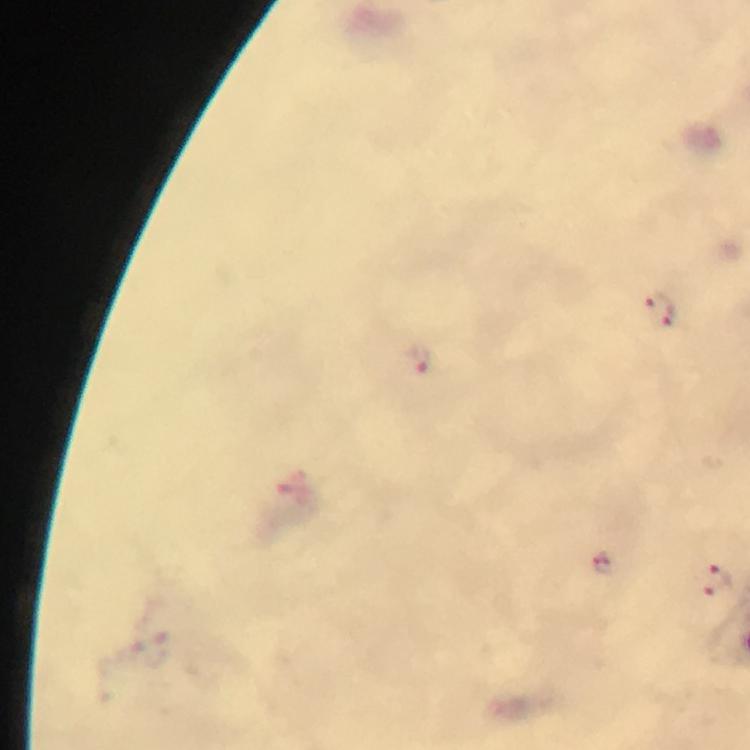

Approximate object centers, in pixels from the top-left corner. Plasmodium parasite locations: (x=658, y=306), (x=420, y=358), (x=603, y=561), (x=715, y=581). From a malaria diagnostic workup. A crop from one field of view. Thick smear. Image is 750×750 pixels. Giemsa-stained preparation. Immersion oil applied. Photographed with a smartphone mounted on the microscope. At 100x magnification.